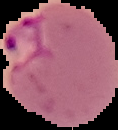
Image is 118×130 pixels. From a thin blood smear. Malaria status: parasitized. The area outside the segmented cell region is set to black.